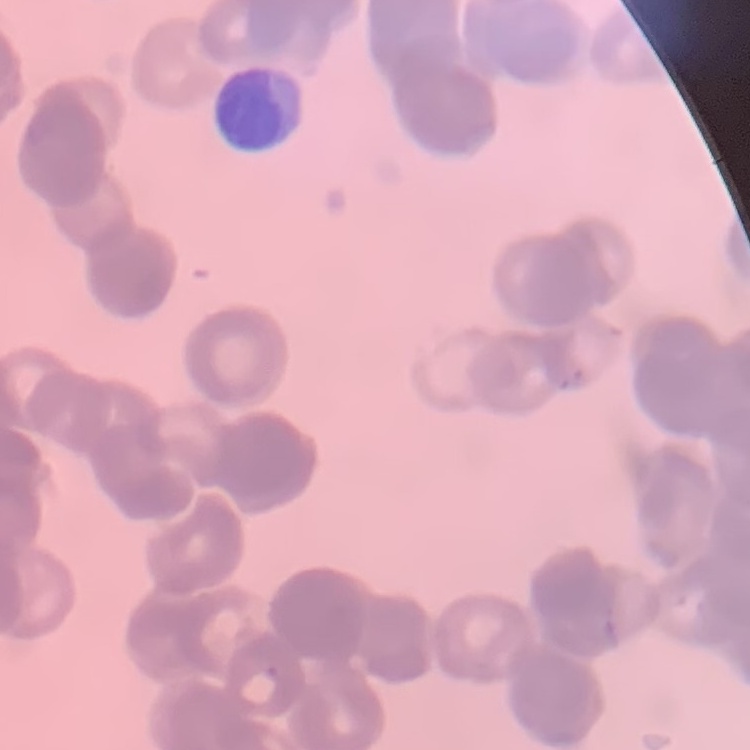
The red blood cells exhibit rouleaux formation. Thin peripheral smear. One tile cut from a larger photomicrograph. Stained with either Field's or Giemsa.